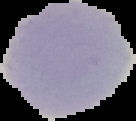

Summary:
  - Preparation: thin blood film
  - Image type: segmented cell region on a black background
  - Result: negative for malaria parasites
  - Image size: 136×121 pixels